Evaluate for Plasmodium parasites.
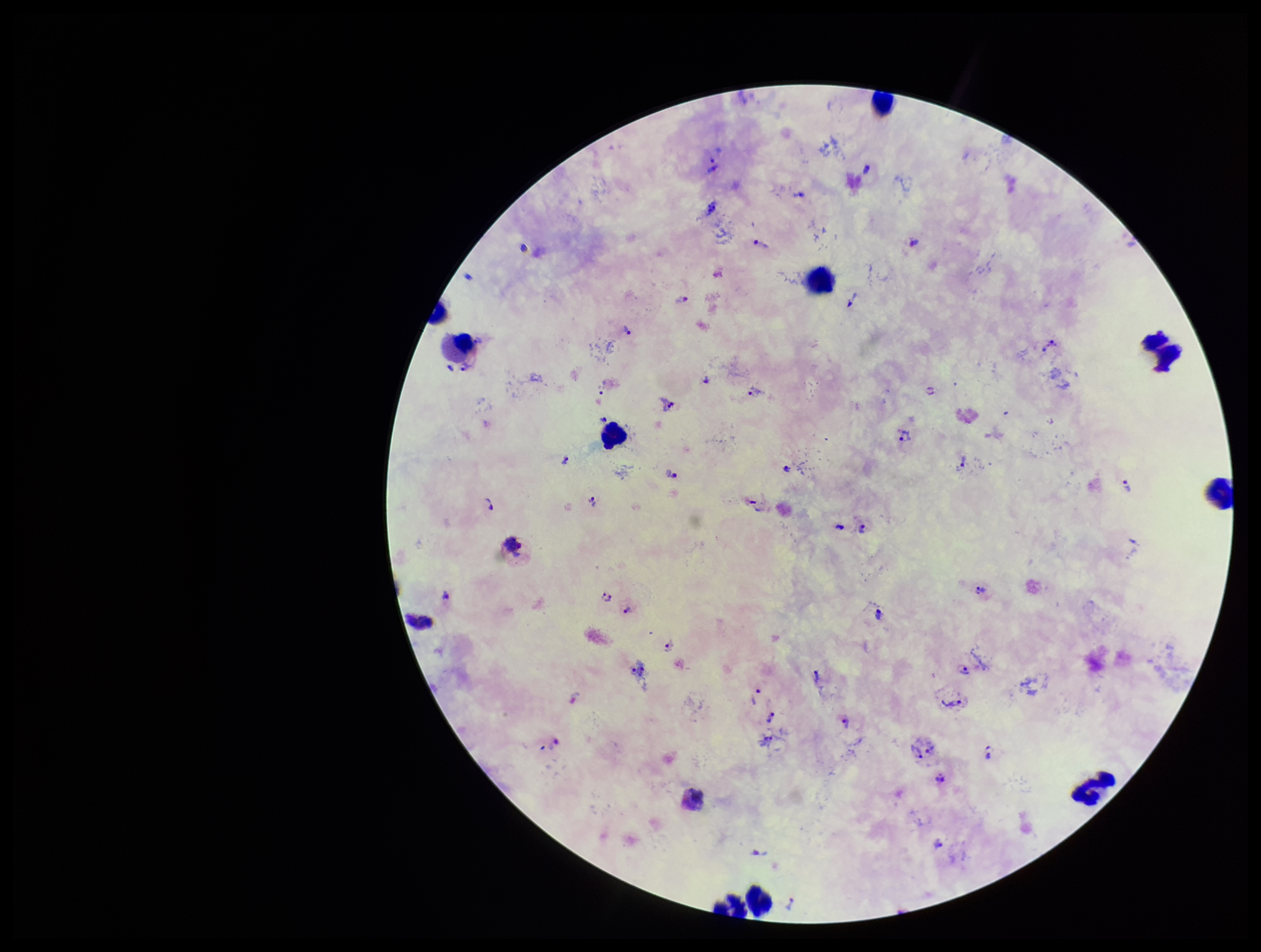
Detected.

image size = 1261×952 pixels
field of view = one from this slide
capture = smartphone photograph through the microscope eyepiece
species reported for this patient = Plasmodium vivax
preparation = thick smear
leukocyte count = 10
stain = Giemsa
patient malaria status = infected
parasite count = 45